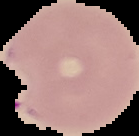
From a thin blood film. The area outside the segmented cell region is set to black. Image is 139×136 pixels. Malaria status: parasitized.